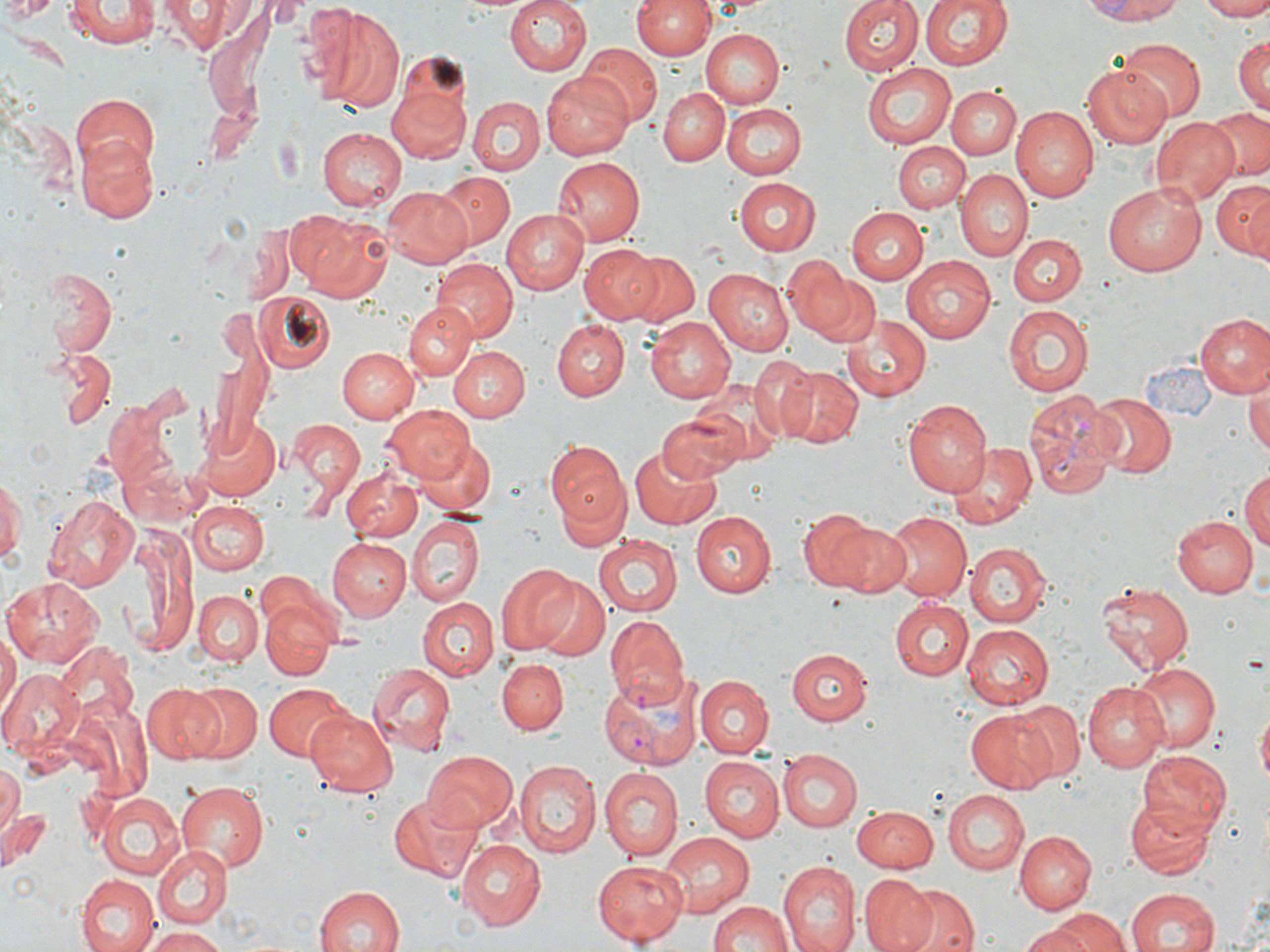
Approximate bounding boxes as named x1/y1/x2/y2 corners in pixels. Plasmodium vivax-infected red blood cell locations: (x1=1023, y1=388, x2=1119, y2=501), (x1=604, y1=614, x2=687, y2=710), (x1=598, y1=671, x2=701, y2=769). Uninfected red blood cell locations: (x1=62, y1=0, x2=159, y2=50), (x1=158, y1=0, x2=251, y2=51), (x1=504, y1=0, x2=591, y2=77), (x1=630, y1=0, x2=715, y2=60), (x1=838, y1=0, x2=923, y2=75), (x1=920, y1=0, x2=1012, y2=72), (x1=1081, y1=0, x2=1191, y2=24), (x1=1193, y1=0, x2=1270, y2=20), (x1=4, y1=1, x2=58, y2=23), (x1=303, y1=4, x2=408, y2=111), (x1=702, y1=29, x2=783, y2=108), (x1=1233, y1=35, x2=1269, y2=113), (x1=1115, y1=41, x2=1207, y2=121), (x1=578, y1=44, x2=660, y2=126), (x1=863, y1=62, x2=956, y2=149), (x1=1082, y1=63, x2=1175, y2=149), (x1=544, y1=72, x2=637, y2=161), (x1=386, y1=85, x2=472, y2=166), (x1=947, y1=85, x2=1022, y2=158), (x1=659, y1=87, x2=729, y2=166), (x1=73, y1=92, x2=160, y2=178), (x1=465, y1=96, x2=543, y2=175), (x1=722, y1=103, x2=806, y2=178), (x1=1010, y1=106, x2=1098, y2=202), (x1=1204, y1=106, x2=1270, y2=182), (x1=1152, y1=116, x2=1240, y2=205), (x1=317, y1=126, x2=408, y2=211), (x1=76, y1=136, x2=159, y2=221), (x1=894, y1=142, x2=969, y2=212), (x1=552, y1=157, x2=644, y2=245), (x1=955, y1=169, x2=1031, y2=263), (x1=432, y1=171, x2=517, y2=251), (x1=731, y1=177, x2=820, y2=255), (x1=1211, y1=180, x2=1270, y2=257), (x1=1102, y1=181, x2=1206, y2=276), (x1=382, y1=186, x2=470, y2=267), (x1=846, y1=207, x2=925, y2=283), (x1=500, y1=208, x2=590, y2=292), (x1=290, y1=210, x2=389, y2=301), (x1=245, y1=219, x2=299, y2=303), (x1=1010, y1=234, x2=1086, y2=308), (x1=581, y1=243, x2=666, y2=325), (x1=620, y1=250, x2=700, y2=328), (x1=780, y1=255, x2=854, y2=334), (x1=899, y1=255, x2=996, y2=343), (x1=434, y1=259, x2=516, y2=341), (x1=42, y1=268, x2=116, y2=357), (x1=704, y1=268, x2=793, y2=356), (x1=813, y1=272, x2=881, y2=349), (x1=255, y1=294, x2=335, y2=372), (x1=403, y1=303, x2=476, y2=380), (x1=1002, y1=304, x2=1093, y2=398), (x1=841, y1=314, x2=934, y2=401), (x1=1196, y1=314, x2=1270, y2=399), (x1=643, y1=316, x2=736, y2=404), (x1=553, y1=320, x2=628, y2=400), (x1=336, y1=346, x2=418, y2=423), (x1=448, y1=347, x2=527, y2=423), (x1=53, y1=351, x2=115, y2=428), (x1=747, y1=357, x2=822, y2=442), (x1=771, y1=364, x2=864, y2=448), (x1=1246, y1=377, x2=1270, y2=458), (x1=687, y1=379, x2=785, y2=466), (x1=1088, y1=392, x2=1176, y2=478), (x1=903, y1=399, x2=991, y2=496), (x1=381, y1=405, x2=474, y2=485), (x1=659, y1=409, x2=748, y2=482), (x1=195, y1=415, x2=280, y2=500), (x1=289, y1=420, x2=364, y2=505), (x1=418, y1=439, x2=495, y2=519), (x1=950, y1=441, x2=1035, y2=527), (x1=549, y1=442, x2=630, y2=533), (x1=628, y1=444, x2=726, y2=532), (x1=1240, y1=468, x2=1270, y2=556), (x1=342, y1=469, x2=423, y2=540), (x1=0, y1=472, x2=23, y2=567), (x1=43, y1=492, x2=141, y2=591), (x1=186, y1=501, x2=269, y2=575), (x1=801, y1=509, x2=893, y2=594), (x1=692, y1=511, x2=776, y2=599), (x1=882, y1=513, x2=969, y2=602), (x1=1171, y1=515, x2=1255, y2=598), (x1=408, y1=517, x2=484, y2=607), (x1=126, y1=526, x2=197, y2=654), (x1=595, y1=534, x2=681, y2=618), (x1=330, y1=538, x2=410, y2=620), (x1=967, y1=542, x2=1051, y2=626), (x1=495, y1=561, x2=579, y2=654), (x1=253, y1=569, x2=336, y2=638), (x1=3, y1=577, x2=103, y2=667), (x1=534, y1=579, x2=607, y2=659), (x1=1095, y1=583, x2=1194, y2=674), (x1=193, y1=591, x2=263, y2=665), (x1=418, y1=597, x2=497, y2=680), (x1=889, y1=599, x2=972, y2=681), (x1=262, y1=603, x2=334, y2=679), (x1=960, y1=622, x2=1053, y2=709), (x1=0, y1=626, x2=18, y2=725), (x1=53, y1=641, x2=138, y2=721), (x1=787, y1=649, x2=871, y2=725), (x1=497, y1=657, x2=568, y2=733), (x1=1132, y1=661, x2=1218, y2=753), (x1=368, y1=662, x2=456, y2=753), (x1=0, y1=669, x2=82, y2=757), (x1=696, y1=676, x2=773, y2=759), (x1=1083, y1=681, x2=1169, y2=772), (x1=185, y1=682, x2=261, y2=761), (x1=262, y1=682, x2=350, y2=760), (x1=143, y1=684, x2=226, y2=763), (x1=1011, y1=701, x2=1083, y2=781), (x1=1257, y1=705, x2=1269, y2=790), (x1=305, y1=708, x2=398, y2=797), (x1=966, y1=708, x2=1060, y2=792), (x1=777, y1=749, x2=862, y2=832), (x1=1137, y1=749, x2=1232, y2=837), (x1=420, y1=751, x2=518, y2=834), (x1=699, y1=756, x2=783, y2=843), (x1=514, y1=761, x2=600, y2=858), (x1=1, y1=765, x2=21, y2=837), (x1=600, y1=770, x2=681, y2=862), (x1=176, y1=781, x2=270, y2=873), (x1=943, y1=788, x2=1027, y2=875), (x1=97, y1=792, x2=184, y2=877), (x1=388, y1=794, x2=480, y2=883), (x1=1125, y1=795, x2=1213, y2=880), (x1=851, y1=805, x2=939, y2=871), (x1=2, y1=808, x2=48, y2=864), (x1=1014, y1=831, x2=1094, y2=914), (x1=661, y1=832, x2=755, y2=915), (x1=456, y1=840, x2=545, y2=928), (x1=152, y1=842, x2=232, y2=928), (x1=593, y1=860, x2=688, y2=945), (x1=776, y1=862, x2=858, y2=952), (x1=859, y1=874, x2=936, y2=952), (x1=76, y1=875, x2=158, y2=952), (x1=900, y1=882, x2=978, y2=952), (x1=312, y1=886, x2=405, y2=952), (x1=1124, y1=886, x2=1220, y2=951), (x1=706, y1=900, x2=793, y2=952), (x1=1035, y1=908, x2=1132, y2=952), (x1=1023, y1=921, x2=1096, y2=952), (x1=141, y1=926, x2=228, y2=951). Slide-level diagnosis: Plasmodium vivax. May-Grünwald-Giemsa-stained preparation. Captured at 1000x magnification. Single field of view. Thin blood film. Image is 1270×952 pixels. Light microscopy.